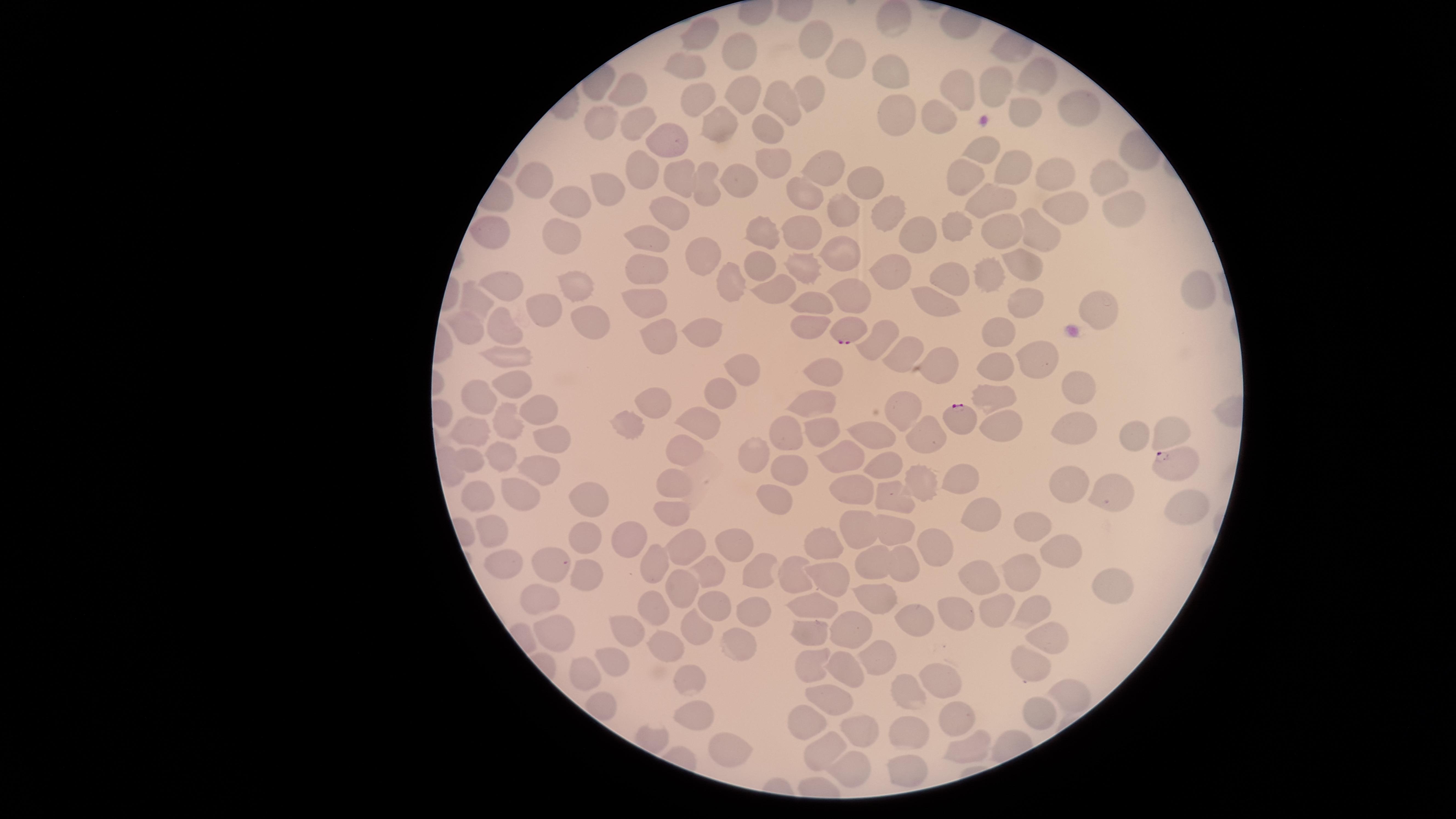
Approximate marker points as (x, y) in pixels. Parasitized RBCs: (847, 330), (961, 418), (1175, 465). Uninfected RBCs: (898, 21), (700, 34), (813, 41), (736, 53), (687, 65), (845, 65), (891, 70), (1040, 77), (997, 87), (626, 88), (961, 88), (813, 89), (737, 90), (691, 97), (779, 105), (1080, 105), (935, 114), (891, 115), (1020, 115), (599, 126), (719, 126), (772, 126), (635, 129), (668, 138), (982, 149), (774, 157), (815, 164), (1015, 164), (638, 170), (540, 175), (682, 175), (1107, 176), (1056, 177), (731, 182), (963, 182), (865, 184), (805, 193), (705, 194), (602, 195), (985, 198), (1121, 204), (565, 205), (676, 208), (885, 209), (1070, 211), (844, 214), (958, 228), (765, 230), (651, 233), (801, 233), (912, 233), (1005, 233), (1045, 234), (491, 236), (558, 237), (842, 250), (699, 259), (1016, 263), (760, 264), (800, 265), (893, 266), (644, 267), (955, 278), (986, 279), (506, 280), (574, 285), (732, 285), (1199, 289), (776, 292), (851, 295), (653, 299), (481, 300), (808, 300), (1024, 301), (541, 304), (937, 304), (1095, 308), (590, 317), (705, 327), (806, 327), (471, 328), (501, 331), (993, 332), (660, 336), (879, 341), (902, 355), (1033, 356), (504, 357), (992, 364), (740, 366), (818, 368), (942, 369), (514, 381), (1077, 393), (482, 396), (994, 400), (717, 401), (815, 406), (655, 408), (545, 414), (904, 415), (504, 424), (699, 424), (627, 425), (1001, 427), (1070, 429), (825, 431), (924, 433), (472, 434), (874, 436), (1133, 436), (1168, 436), (551, 439), (781, 440), (683, 450), (845, 453), (756, 455), (500, 457), (469, 458), (789, 465), (882, 469), (539, 471), (963, 479), (676, 485), (921, 486), (851, 489), (1060, 489), (779, 492), (891, 492), (1103, 493), (474, 498), (519, 498), (590, 500), (1176, 508), (673, 515), (977, 517), (1031, 524), (894, 530), (856, 532), (489, 536), (625, 537), (582, 539), (818, 543), (728, 546), (935, 546), (685, 548), (1065, 551), (655, 560), (552, 561), (875, 561), (499, 562), (901, 567), (1021, 569), (757, 570), (788, 573), (706, 575), (823, 577), (587, 580), (976, 582), (1109, 584), (675, 590), (542, 599), (878, 599), (708, 604), (996, 606), (650, 607), (752, 607), (1030, 608), (813, 609), (959, 609), (916, 620), (852, 628), (806, 629), (688, 630), (551, 633), (619, 635), (1055, 639), (664, 648), (735, 652), (815, 658), (612, 660), (877, 660), (1031, 662), (841, 664), (580, 676), (688, 676), (935, 683), (824, 693), (1075, 694), (903, 696), (697, 714), (1034, 716), (810, 721), (952, 721), (857, 728), (906, 736), (967, 749), (726, 751), (828, 753), (907, 765), (856, 771). Smartphone photograph through the microscope eyepiece. Species: Plasmodium falciparum. Giemsa-stained preparation. Image is 1456×819 pixels. Thin blood smear. Single field of view. The visible region is circular. Presence: malaria parasites identified.